Name the parasite shown.
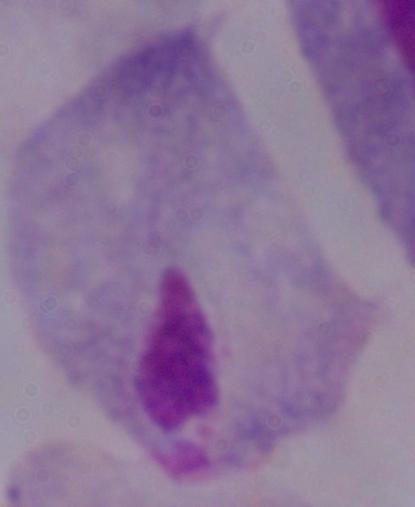

This is a trichomonad.

Micrograph. 1000x magnification.